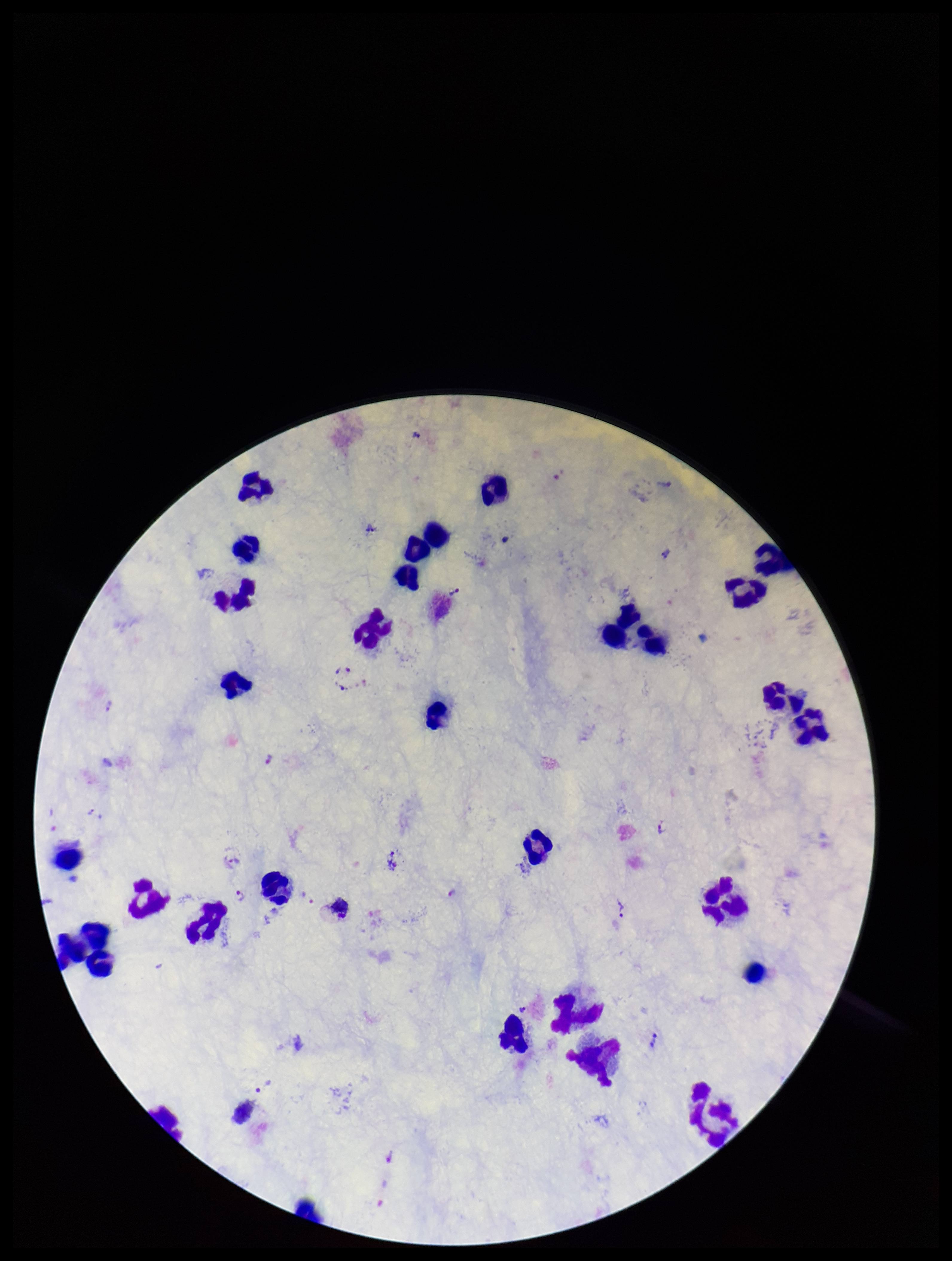

Smartphone photograph taken through the eyepiece of a microscope. Leukocyte count: 29. Preparation: thick. One field from this slide. Species reported for this patient: Plasmodium vivax. Image is 952×1261 pixels. Stained with Giemsa. Plasmodium parasites: seen. Patient malaria status: positive. Parasite count: 12.